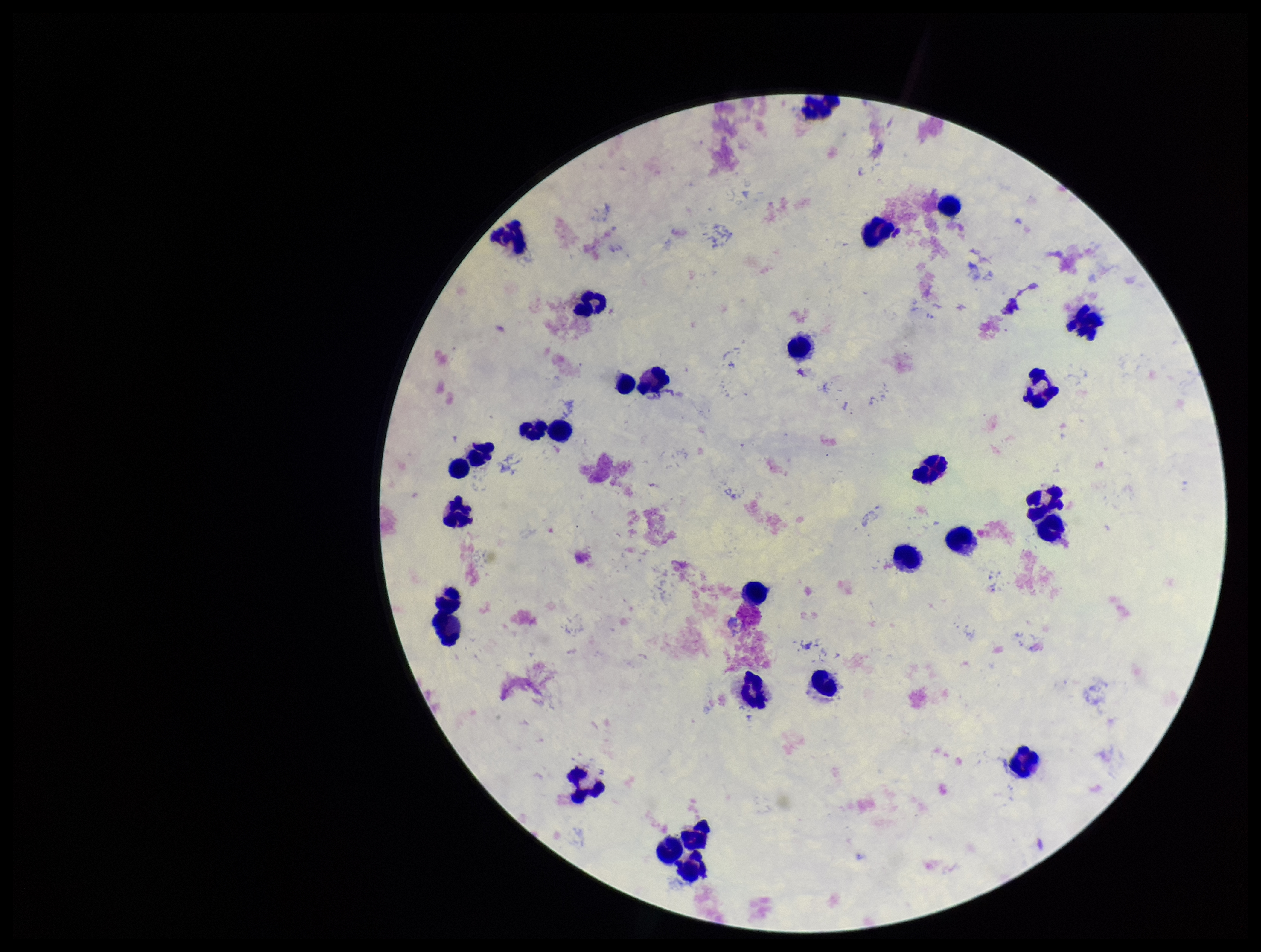

Summary:
  - Stain: Giemsa
  - Image size: 1261×952 pixels
  - Patient malaria status: negative
  - Leukocyte count: 29
  - Field of view: one from this slide
  - Plasmodium parasites: none seen
  - Parasite count: 0
  - Preparation: thick
  - Capture: smartphone photograph through the microscope eyepiece